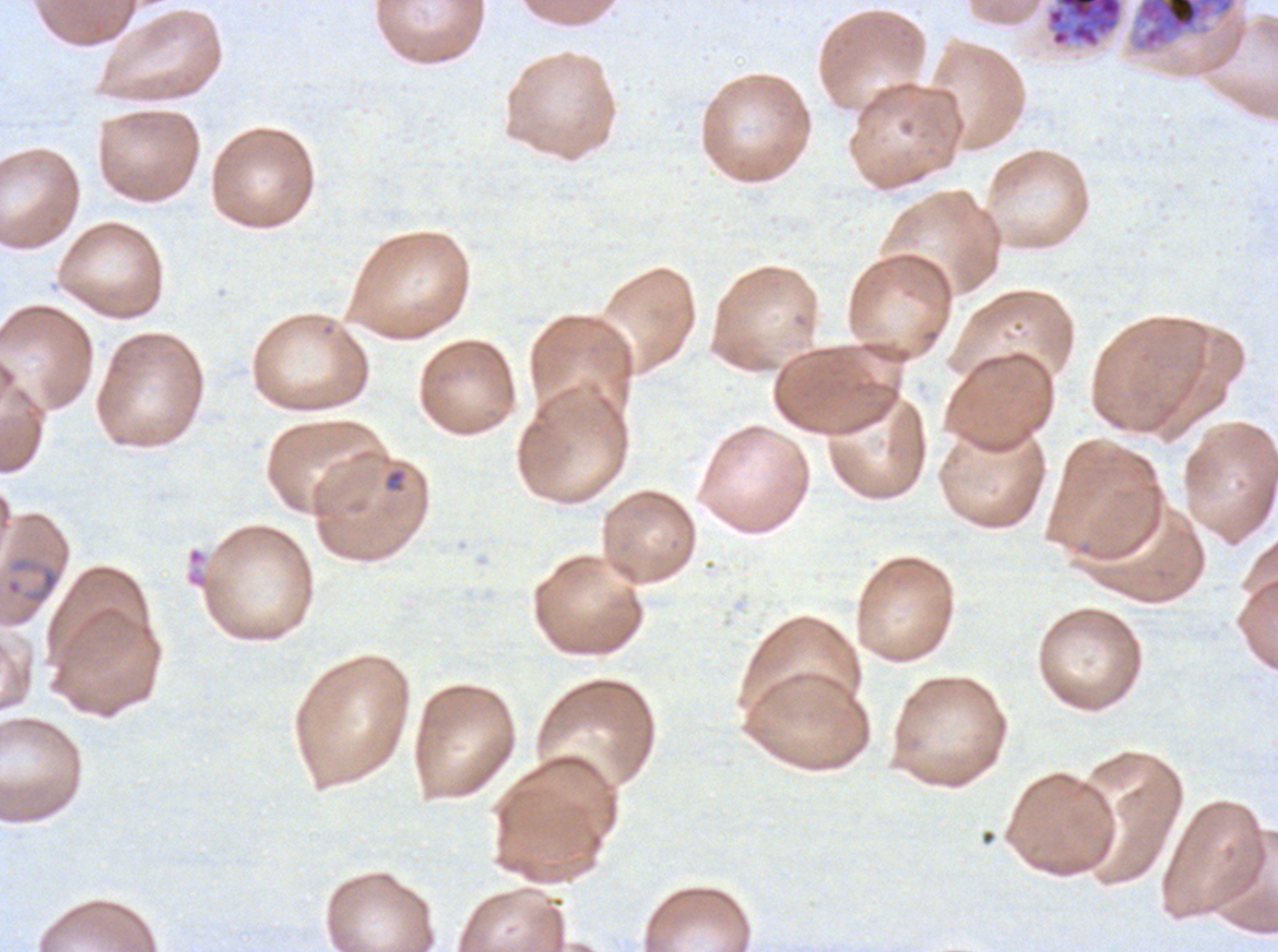
Approximate bounding boxes as [x1, y1, x2, y2] in pixels. Late schizont locations: [1129, 0, 1237, 53]. Segmenter locations: [1046, 0, 1124, 48]. Ring locations: [384, 468, 406, 493], [5, 555, 62, 607]. Giemsa-stained preparation. Ex-vivo Plasmodium falciparum culture from a patient in The Gambia, grown for 24 to 48 hours. Life-cycle stages observed: ring, late schizont, segmenter. Image is 1278×952 pixels. A sub-image separated from a larger composite. Thin blood film.